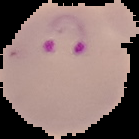
result = malaria parasites identified
preparation = thin blood smear
image type = segmented cell region on a black background
image size = 139×139 pixels